Locate every Plasmodium vivax-infected red blood cell.
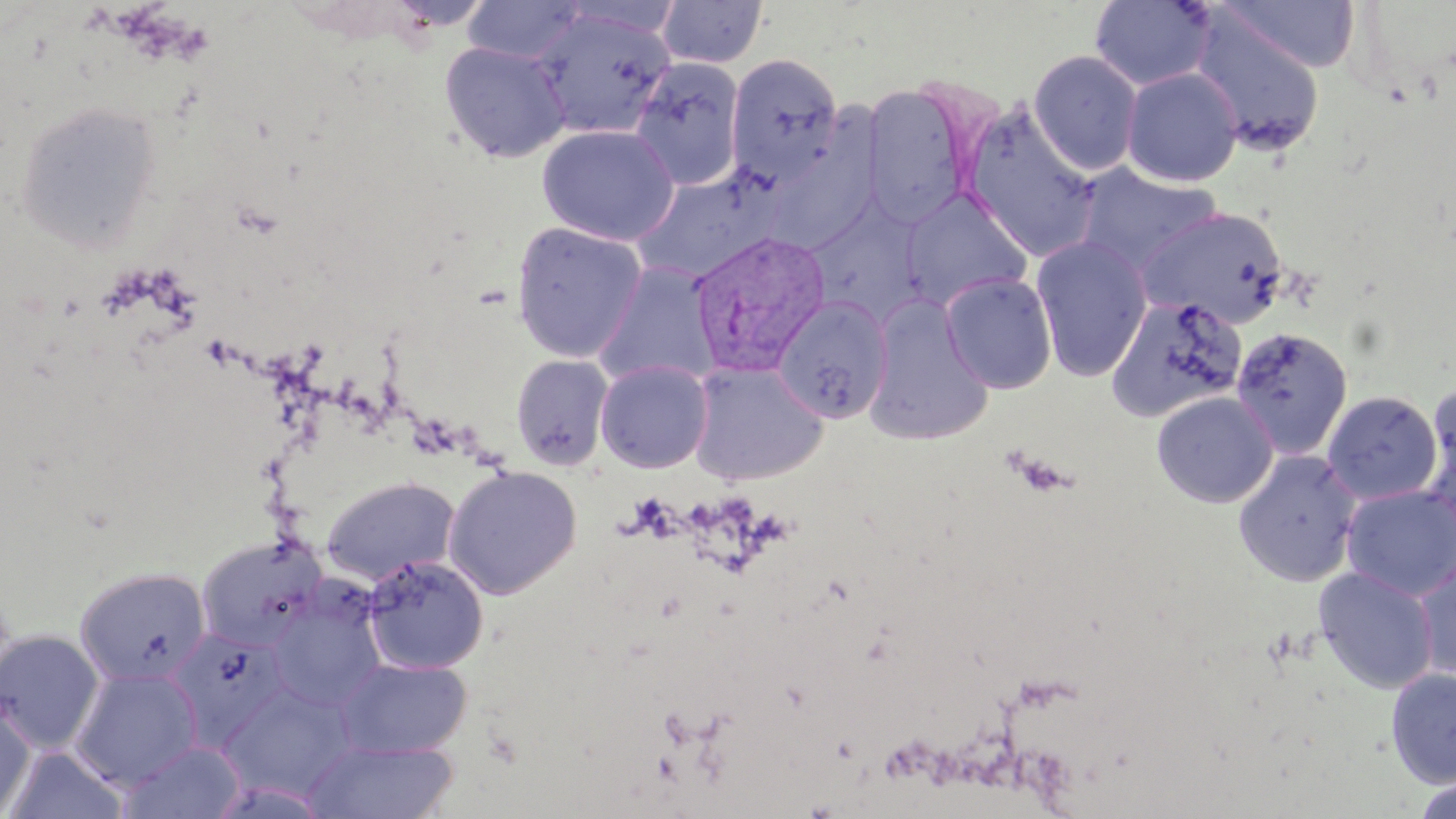

Approximate bounding boxes as [x1, y1, x2, y2] in pixels.
Plasmodium vivax-infected red blood cells: [688, 229, 830, 375].

Uninfected red blood cell locations: [461, 0, 588, 64], [657, 0, 768, 69], [1090, 0, 1216, 90], [1219, 0, 1360, 73], [532, 7, 675, 139], [1187, 9, 1326, 157], [439, 41, 571, 163], [1028, 50, 1143, 176], [725, 53, 844, 185], [630, 58, 745, 190], [1121, 67, 1243, 187], [862, 85, 976, 226], [15, 100, 161, 251], [959, 103, 1100, 262], [537, 125, 679, 246], [760, 134, 882, 255], [1074, 162, 1225, 272], [631, 167, 781, 283], [900, 187, 1034, 310], [804, 204, 925, 327], [1137, 206, 1288, 329], [511, 221, 648, 363], [1030, 234, 1153, 381], [593, 261, 722, 388], [940, 271, 1059, 394], [1106, 293, 1248, 422], [862, 295, 994, 447], [772, 297, 894, 423], [1230, 325, 1354, 459], [510, 354, 614, 471], [595, 359, 714, 473], [688, 360, 828, 485], [1421, 388, 1456, 529], [1150, 390, 1279, 508], [1322, 390, 1442, 505], [1232, 448, 1362, 587], [443, 465, 582, 599], [321, 476, 460, 585], [1341, 484, 1456, 600], [195, 534, 327, 653], [1412, 553, 1456, 681], [361, 554, 488, 675], [74, 566, 211, 688], [1314, 566, 1439, 694], [266, 584, 388, 714], [166, 626, 288, 746], [0, 629, 104, 753], [337, 658, 472, 757], [70, 667, 203, 790], [1386, 667, 1456, 789], [221, 690, 355, 804], [0, 698, 35, 815], [303, 738, 459, 819], [118, 741, 247, 819], [4, 745, 129, 819], [1411, 776, 1455, 819]. Slide-level diagnosis: Plasmodium vivax. Thin blood smear. May-Grünwald-Giemsa-stained preparation. Captured at 1000x magnification. Optical microscopy. Image is 1456×819 pixels. One field of a larger specimen.